Locate every blood parasite and identify its species.
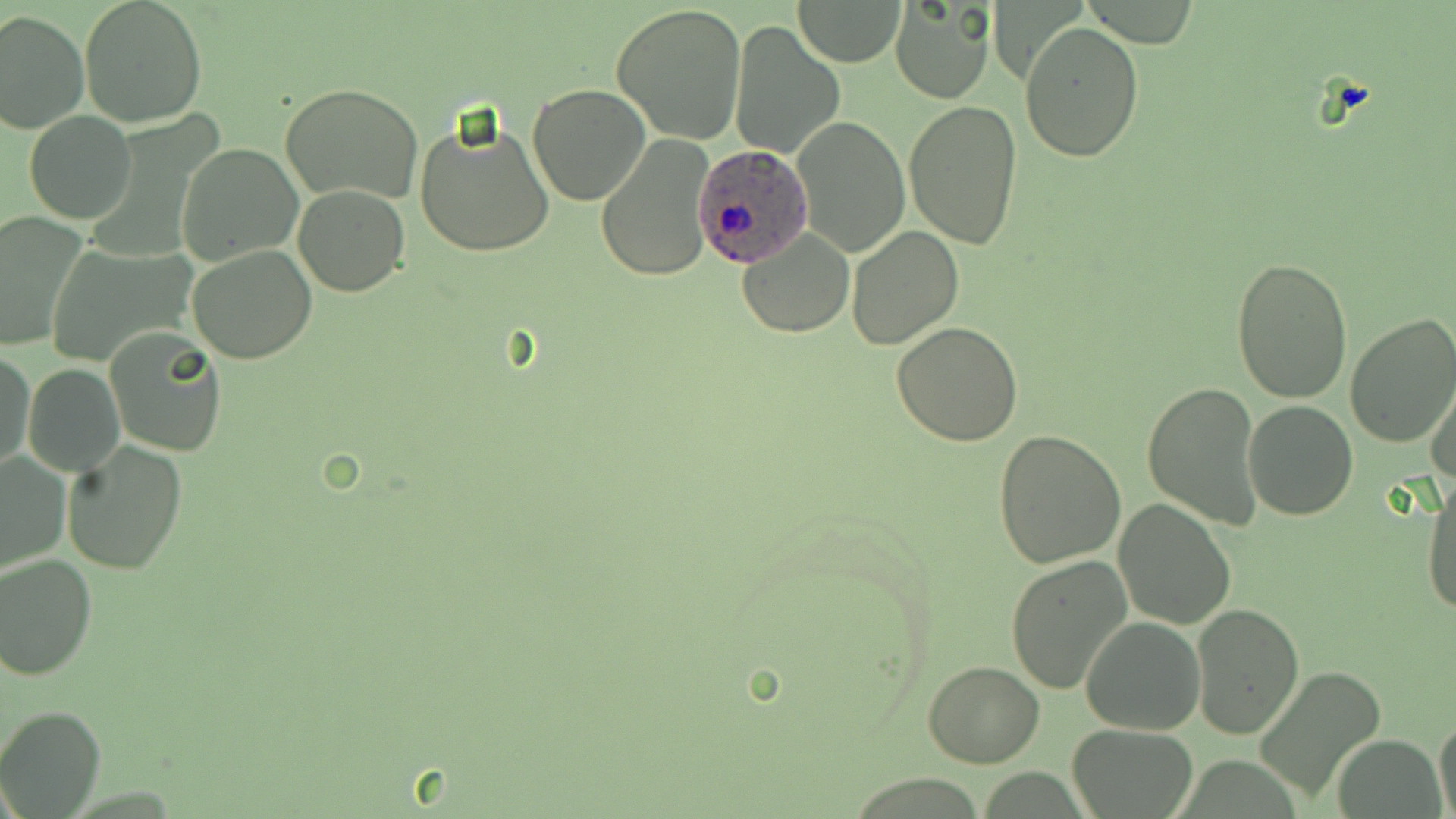

Approximate bounding boxes as [x1, y1, x2, y2] in pixels.
Plasmodium ovale-infected red blood cells: [692, 149, 812, 264].
No Plasmodium falciparum, Plasmodium malariae, Plasmodium vivax, Babesia divergens, or Trypanosoma brucei observed.

Uninfected red blood cell locations: [78, 0, 208, 128], [793, 0, 907, 66], [889, 1, 996, 105], [612, 2, 747, 144], [0, 10, 88, 133], [730, 20, 846, 158], [1021, 22, 1144, 163], [281, 81, 424, 205], [528, 84, 649, 205], [904, 100, 1023, 249], [25, 112, 136, 225], [411, 115, 558, 258], [791, 115, 909, 257], [595, 135, 717, 283], [177, 143, 300, 265], [293, 184, 409, 296], [0, 210, 88, 353], [846, 225, 964, 349], [736, 228, 854, 337], [43, 243, 196, 369], [187, 244, 317, 365], [1230, 256, 1354, 404], [1344, 313, 1456, 449], [891, 323, 1023, 445], [104, 328, 228, 456], [1, 350, 35, 475], [23, 363, 125, 476], [1426, 368, 1456, 490], [1142, 380, 1264, 528], [1243, 399, 1359, 520], [992, 429, 1128, 569], [62, 440, 187, 574], [0, 450, 71, 574], [1421, 475, 1455, 621], [1113, 498, 1237, 628], [1, 553, 98, 682], [1005, 554, 1132, 695], [1191, 604, 1303, 737], [1080, 615, 1205, 735], [922, 661, 1045, 768], [1258, 665, 1387, 801], [0, 705, 105, 817], [1433, 715, 1456, 818], [1068, 723, 1199, 817], [1334, 733, 1443, 819]. Slide-level diagnosis: Plasmodium ovale. Image is 1456×819 pixels. Optical microscopy. Single field of view. Thin blood film. Captured at 1000x magnification. May-Grünwald-Giemsa-stained preparation.